Name the blood parasite species.
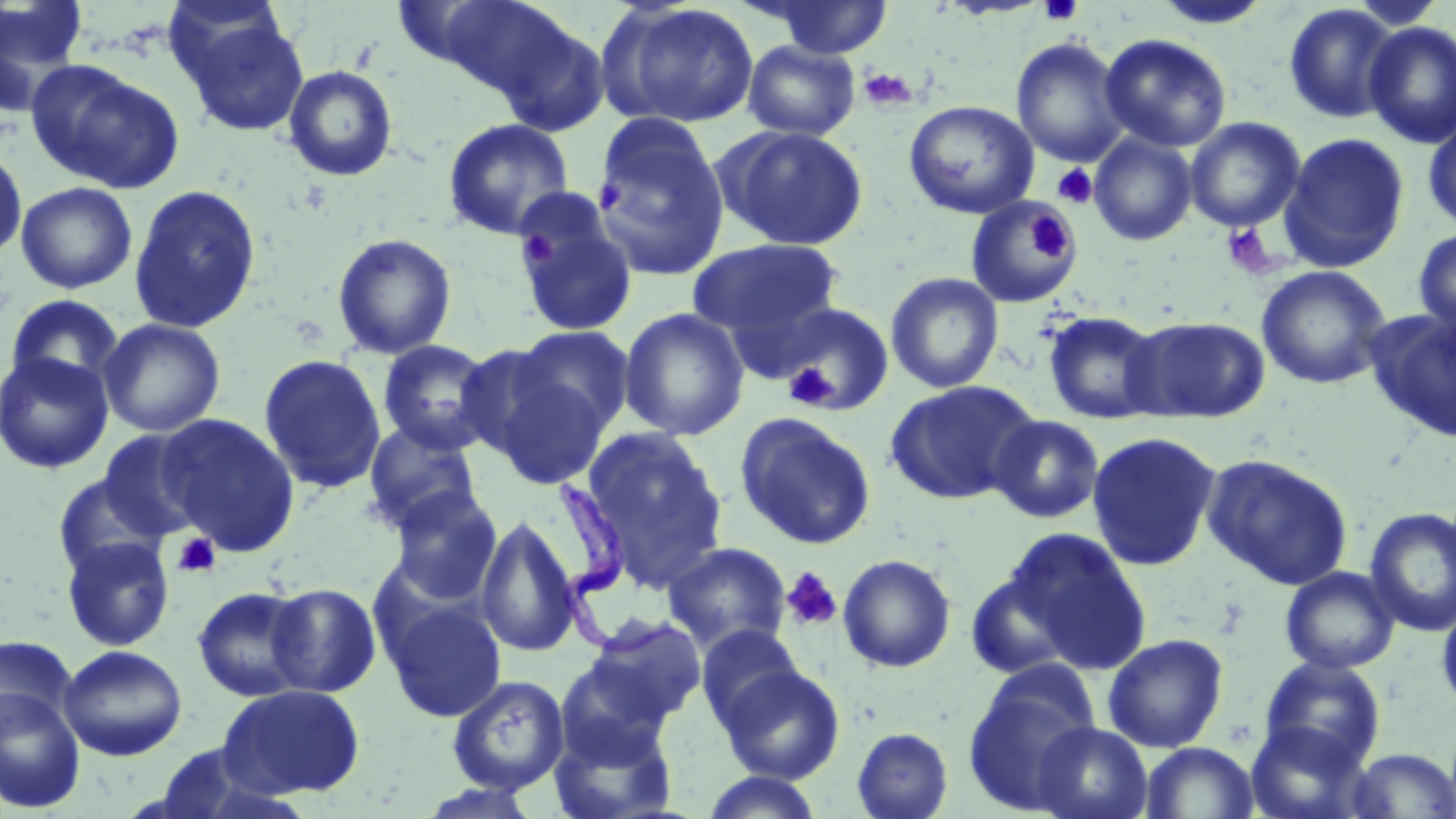

Trypanosoma brucei.

{
  "stain": "May-Grünwald-Giemsa",
  "platelet_locations": "approximate bounding boxes as (x1,y1)-(x2,y2) corner pairs in pixels: (1037,0)-(1085,27), (857,67)-(917,111), (1052,164)-(1098,208), (594,180)-(626,213), (1028,215)-(1074,260), (1220,223)-(1277,279), (518,230)-(556,267), (785,364)-(837,408), (172,532)-(221,578), (780,567)-(843,632)",
  "magnification": "1000x",
  "modality": "optical microscopy",
  "trypanosoma_brucei_locations": "approximate bounding boxes as (x1,y1)-(x2,y2) corner pairs in pixels: (554,475)-(692,659)",
  "image_size": "1456×819 pixels",
  "preparation": "thin blood film",
  "field_of_view": "single",
  "uninfected_red_blood_cell_locations": "approximate bounding boxes as (x1,y1)-(x2,y2) corner pairs in pixels: (0,0)-(91,103), (408,0)-(573,97), (756,0)-(895,59), (1152,1)-(1273,30), (602,2)-(760,128), (1282,3)-(1402,124), (174,11)-(310,136), (486,14)-(614,136), (1362,20)-(1456,148), (1099,33)-(1232,153), (1010,37)-(1131,168), (742,40)-(860,141), (28,60)-(184,194), (282,65)-(399,182), (904,99)-(1040,219), (1423,112)-(1456,236), (1184,116)-(1306,233), (442,117)-(575,240), (592,117)-(730,281), (720,125)-(868,251), (1088,132)-(1198,246), (1278,132)-(1410,272), (0,144)-(27,261), (16,181)-(138,294), (128,183)-(262,334), (965,196)-(1080,309), (512,197)-(637,338), (1413,226)-(1456,338), (331,233)-(457,360), (689,238)-(843,343), (1256,265)-(1392,390), (885,272)-(1004,394), (4,293)-(126,395), (772,302)-(895,416), (618,307)-(749,441), (1364,307)-(1456,443), (1042,310)-(1165,425), (1126,315)-(1270,423), (98,318)-(226,437), (513,325)-(635,436), (377,339)-(498,455), (452,343)-(580,466), (0,351)-(114,474), (258,354)-(387,495), (482,365)-(614,491), (884,379)-(1041,505), (734,411)-(876,549), (157,413)-(300,556), (988,414)-(1105,524), (362,420)-(483,534), (580,428)-(727,591), (98,429)-(208,542), (1086,431)-(1222,571), (1201,453)-(1355,590), (51,473)-(171,582), (386,487)-(503,605), (1364,507)-(1456,637), (476,514)-(582,657), (1002,527)-(1152,675), (61,535)-(175,651), (662,541)-(792,655), (837,554)-(957,673), (1280,566)-(1400,674), (965,571)-(1077,680), (265,583)-(382,697), (192,586)-(311,702), (1436,594)-(1456,717), (384,598)-(507,722), (584,615)-(707,727), (696,624)-(805,732), (1103,633)-(1229,753), (0,635)-(77,737), (58,644)-(187,760), (1258,655)-(1387,770), (556,657)-(674,766), (716,662)-(846,785), (963,672)-(1100,812), (447,674)-(570,795), (218,683)-(366,799), (0,686)-(86,814), (548,713)-(679,818), (1032,721)-(1153,819), (1243,721)-(1370,819), (851,727)-(954,819), (1139,741)-(1260,818), (150,745)-(287,818), (1347,748)-(1455,818), (698,771)-(826,819), (413,783)-(547,819)"
}